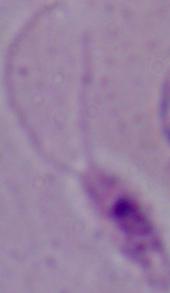

magnification = 1000x
modality = photomicrograph
identification = Leishmania